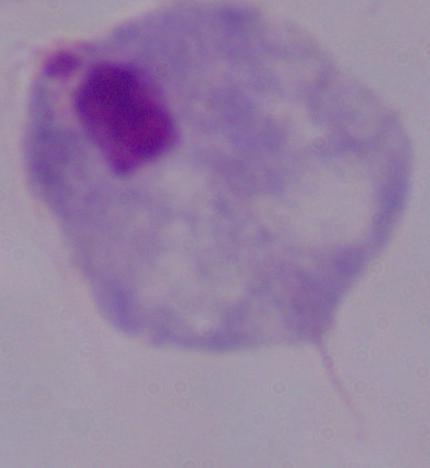 1000x magnification. Photomicrograph. A trichomonad is shown.